Outline each blood parasite and name the species.
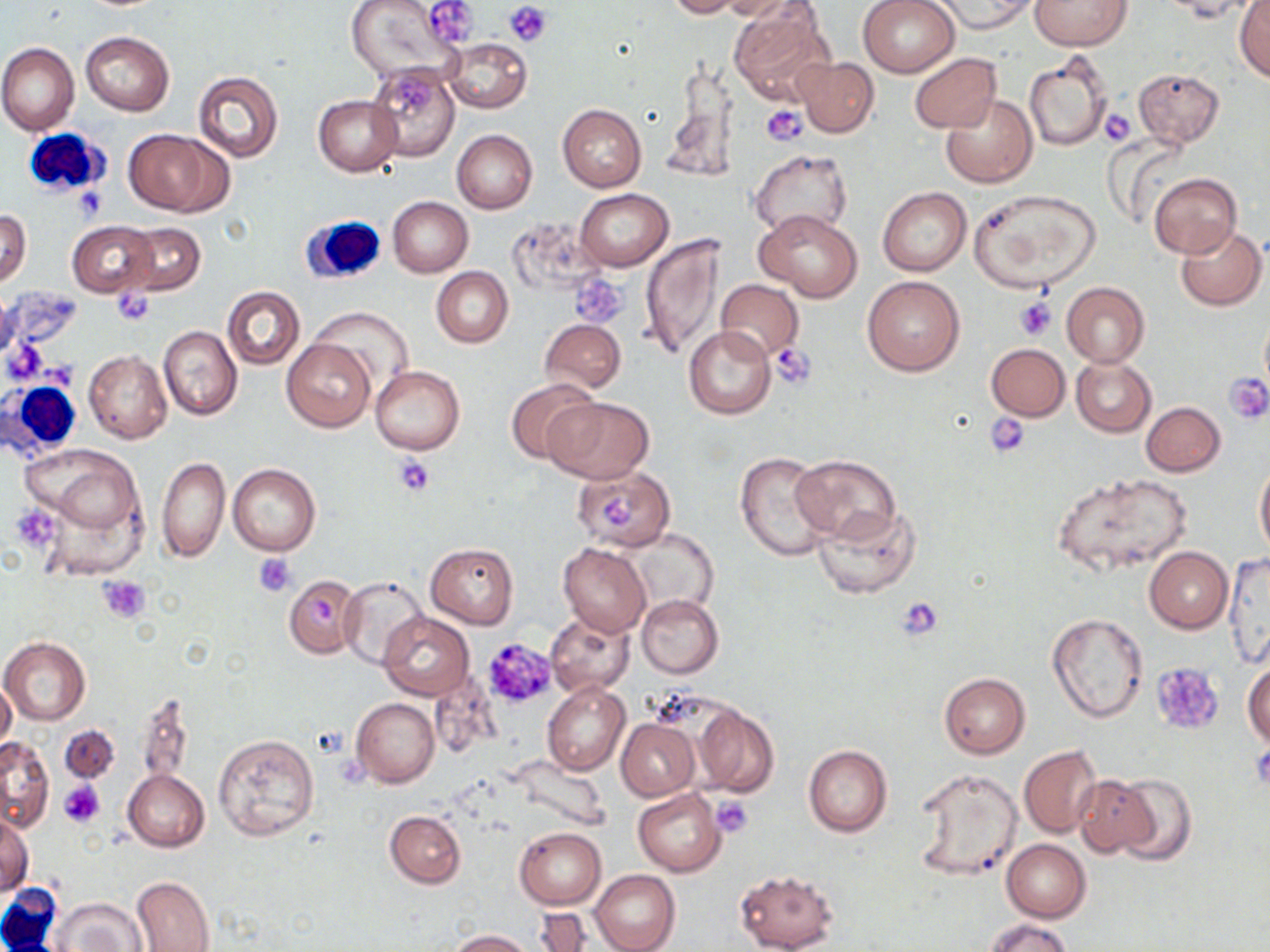

No blood parasites seen.

Approximate bounding boxes as [x1, y1, x2, y2] in pixels. Platelet locations: [506, 1, 553, 46], [425, 2, 478, 44], [394, 77, 434, 110], [763, 106, 805, 146], [1098, 108, 1135, 146], [74, 184, 109, 221], [571, 273, 628, 328], [113, 290, 155, 325], [1015, 297, 1056, 340], [769, 342, 817, 388], [1224, 372, 1270, 424], [985, 413, 1031, 458], [395, 456, 435, 497], [14, 508, 60, 545], [254, 553, 296, 596], [96, 574, 150, 623], [896, 595, 944, 642], [481, 638, 557, 711], [1152, 662, 1221, 732], [59, 781, 105, 829], [713, 796, 754, 838]. White blood cell locations: [22, 125, 113, 200], [299, 215, 386, 286], [3, 377, 86, 459], [1, 885, 63, 951]. Uninfected red blood cell locations: [420, 0, 479, 50], [664, 0, 746, 18], [717, 0, 799, 21], [857, 0, 962, 77], [929, 0, 1035, 35], [1031, 0, 1132, 51], [1157, 0, 1261, 22], [344, 1, 463, 85], [1233, 1, 1270, 81], [730, 4, 836, 107], [81, 32, 174, 115], [443, 37, 531, 114], [1, 43, 79, 136], [1023, 50, 1114, 151], [909, 52, 1001, 133], [794, 57, 879, 136], [368, 65, 460, 162], [666, 66, 739, 181], [1132, 68, 1224, 147], [192, 71, 284, 162], [942, 93, 1037, 187], [313, 95, 402, 175], [557, 105, 646, 191], [124, 128, 230, 216], [451, 130, 538, 214], [750, 151, 852, 237], [1149, 172, 1241, 259], [877, 186, 971, 276], [574, 188, 673, 271], [970, 188, 1100, 291], [388, 196, 473, 277], [1, 208, 32, 286], [755, 208, 862, 301], [68, 221, 160, 298], [1175, 222, 1268, 312], [122, 223, 205, 295], [640, 233, 726, 361], [431, 268, 513, 347], [862, 274, 965, 376], [716, 279, 804, 361], [1061, 281, 1150, 367], [222, 286, 305, 370], [314, 308, 414, 392], [540, 319, 626, 394], [158, 325, 242, 420], [684, 325, 776, 419], [282, 337, 375, 432], [986, 343, 1070, 420], [84, 351, 172, 443], [1070, 356, 1156, 437], [371, 365, 465, 454], [505, 377, 601, 466], [543, 397, 652, 483], [1140, 401, 1225, 476], [19, 442, 148, 561], [735, 452, 834, 562], [790, 454, 900, 543], [158, 457, 228, 562], [1255, 461, 1270, 558], [228, 463, 321, 557], [572, 465, 677, 550], [1052, 471, 1193, 576], [812, 501, 920, 600], [626, 530, 719, 618], [426, 542, 519, 628], [559, 543, 650, 637], [1145, 547, 1233, 632], [1221, 554, 1270, 670], [283, 576, 359, 659], [339, 577, 429, 668], [637, 595, 723, 677], [547, 612, 635, 697], [378, 613, 473, 699], [1047, 613, 1148, 722], [1, 638, 91, 724], [1243, 658, 1270, 750], [938, 672, 1030, 758], [0, 677, 16, 754], [542, 683, 629, 775], [136, 690, 195, 787], [351, 698, 440, 787], [692, 704, 778, 797], [622, 715, 709, 875], [615, 719, 699, 799], [61, 725, 118, 783], [214, 733, 318, 841], [1, 737, 54, 832], [803, 744, 893, 837], [1019, 747, 1101, 837], [503, 755, 609, 831], [912, 768, 1022, 882], [122, 771, 209, 852], [1112, 773, 1197, 866], [1075, 776, 1156, 857], [633, 788, 725, 876], [385, 810, 465, 888], [1, 816, 33, 897], [514, 827, 607, 909], [1001, 840, 1090, 921], [733, 868, 839, 951], [592, 870, 681, 952], [131, 877, 216, 951], [53, 897, 145, 950], [529, 910, 598, 951], [986, 917, 1072, 952], [447, 929, 531, 951]. Slide-level diagnosis: negative for blood parasites. Single field of view. Optical microscopy. Captured at 1000x magnification. Image is 1270×952 pixels. Thin blood smear. May-Grünwald-Giemsa-stained preparation.